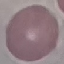

Summary:
  - Result: no malaria parasites seen
  - Image type: automatically extracted cell patch, resized to 64 × 64 pixels
  - Stain: Giemsa
  - Preparation: thin blood film
  - Capture: smartphone camera at the microscope eyepiece